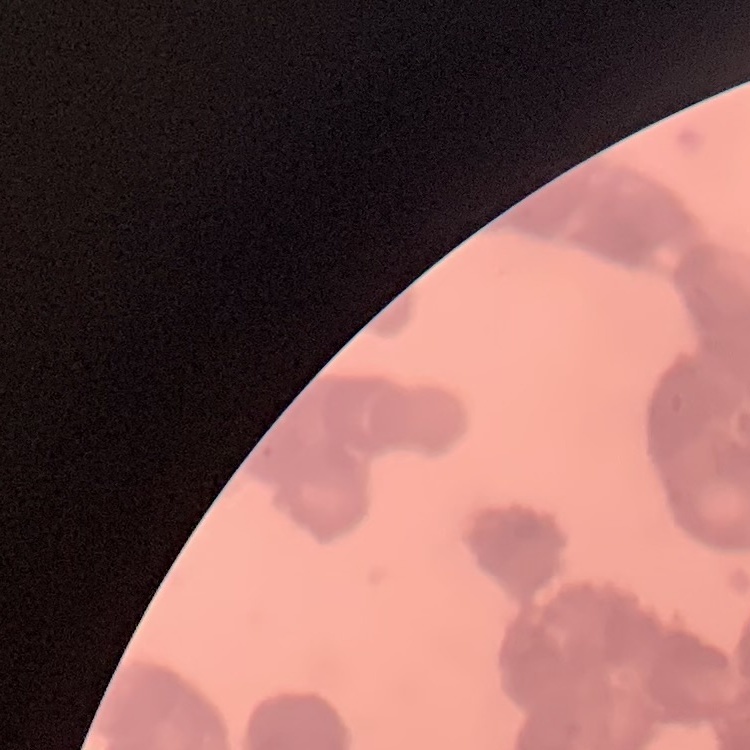 The erythrocytes show rouleaux formation. One tile cut from a larger photomicrograph. Thin blood film. Field's or Giemsa stain.